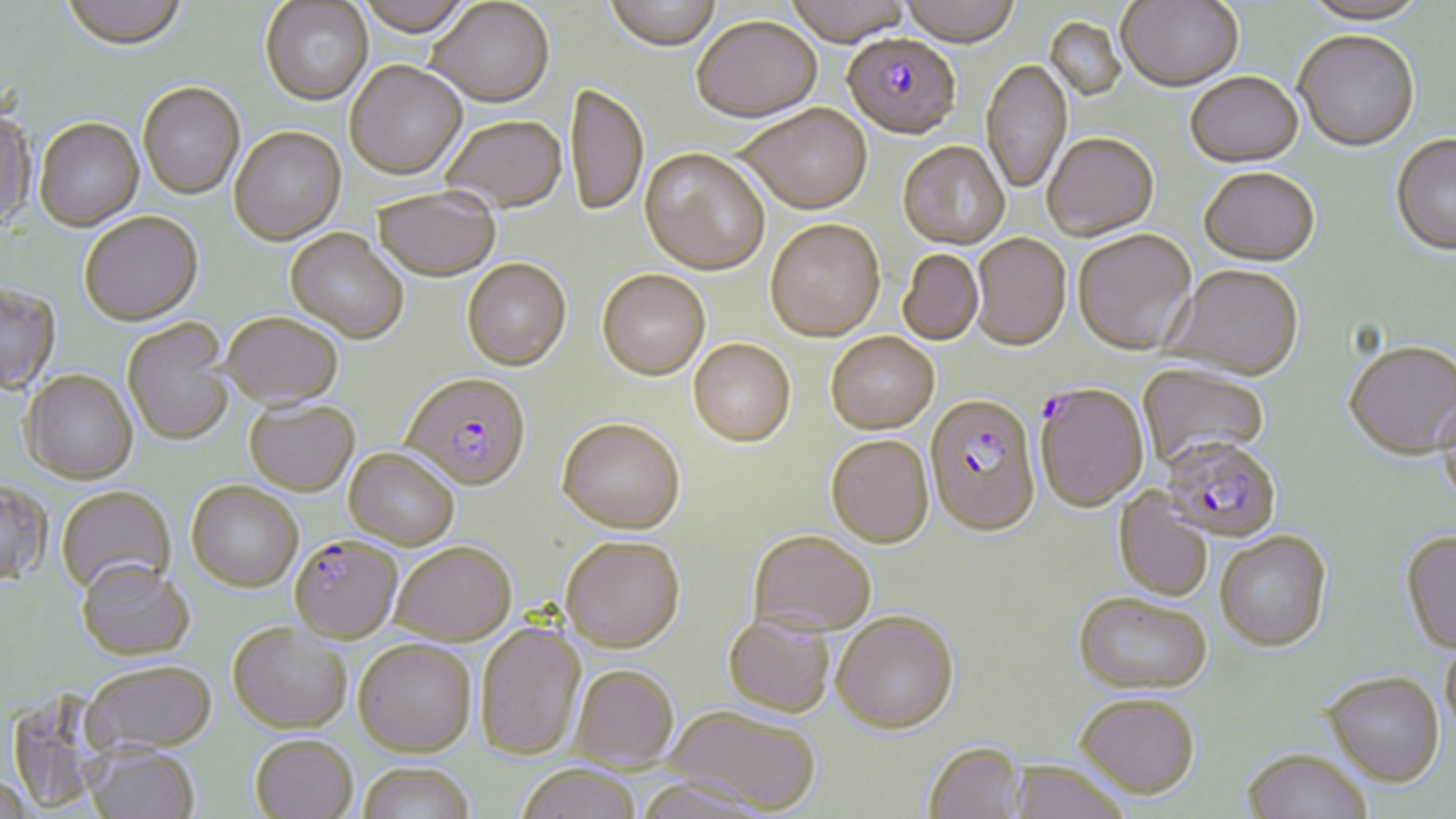

Summary:
  - Coordinate format: approximate bounding boxes as (x1, y1, x2, y2) in pixels
  - Plasmodium falciparum-infected red blood cell locations: (842, 36, 961, 143), (402, 375, 531, 493), (1034, 385, 1149, 515), (925, 398, 1041, 541), (1164, 435, 1288, 545), (290, 538, 402, 647)
  - Uninfected red blood cell locations: (60, 0, 188, 53), (353, 0, 475, 42), (604, 0, 722, 53), (784, 0, 914, 50), (900, 0, 1019, 51), (1116, 0, 1243, 95), (1301, 1, 1430, 29), (260, 2, 373, 108), (425, 2, 554, 111), (1044, 18, 1126, 102), (692, 19, 822, 126), (1294, 34, 1419, 154), (981, 61, 1073, 196), (344, 63, 467, 182), (1185, 75, 1304, 171), (138, 84, 245, 201), (567, 85, 649, 219), (738, 108, 872, 218), (0, 111, 35, 234), (441, 117, 567, 215), (34, 120, 144, 233), (229, 128, 346, 246), (1043, 136, 1159, 242), (1391, 136, 1456, 259), (898, 144, 1010, 251), (639, 150, 769, 278), (1199, 170, 1320, 269), (372, 191, 501, 284), (79, 214, 204, 328), (765, 222, 885, 344), (285, 230, 408, 345), (1073, 231, 1197, 357), (971, 235, 1071, 353), (898, 250, 983, 346), (462, 261, 571, 373), (1162, 267, 1305, 383), (597, 272, 710, 383), (0, 283, 61, 396), (221, 315, 344, 412), (122, 320, 235, 447), (825, 335, 939, 437), (688, 341, 796, 450), (1344, 344, 1455, 463), (1137, 364, 1269, 473), (21, 372, 137, 486), (1436, 393, 1456, 513), (245, 401, 360, 498), (556, 421, 684, 537), (826, 438, 934, 551), (344, 450, 459, 551), (0, 481, 53, 589), (186, 483, 303, 594), (56, 487, 176, 600), (1113, 487, 1214, 602), (748, 533, 876, 640), (1215, 533, 1333, 655), (1401, 534, 1456, 656), (560, 539, 685, 656), (390, 545, 516, 647), (77, 564, 195, 663), (1072, 595, 1211, 698), (831, 615, 959, 738), (722, 617, 834, 720), (475, 623, 587, 762), (228, 625, 352, 736), (1440, 636, 1456, 740), (353, 642, 476, 761), (83, 665, 217, 760), (569, 667, 679, 773), (1322, 672, 1444, 789), (4, 688, 117, 814), (1075, 696, 1199, 801), (662, 707, 820, 816), (250, 738, 358, 819), (923, 743, 1025, 819), (84, 748, 201, 819), (1241, 750, 1372, 819), (1008, 763, 1130, 819), (516, 765, 641, 819), (357, 766, 475, 819), (0, 777, 38, 819), (634, 778, 773, 819)
  - Slide-level diagnosis: Plasmodium falciparum
  - Preparation: thin blood smear
  - Stain: May-Grünwald-Giemsa
  - Field of view: one of a larger specimen
  - Modality: optical microscopy
  - Image size: 1456×819 pixels
  - Magnification: 1000x